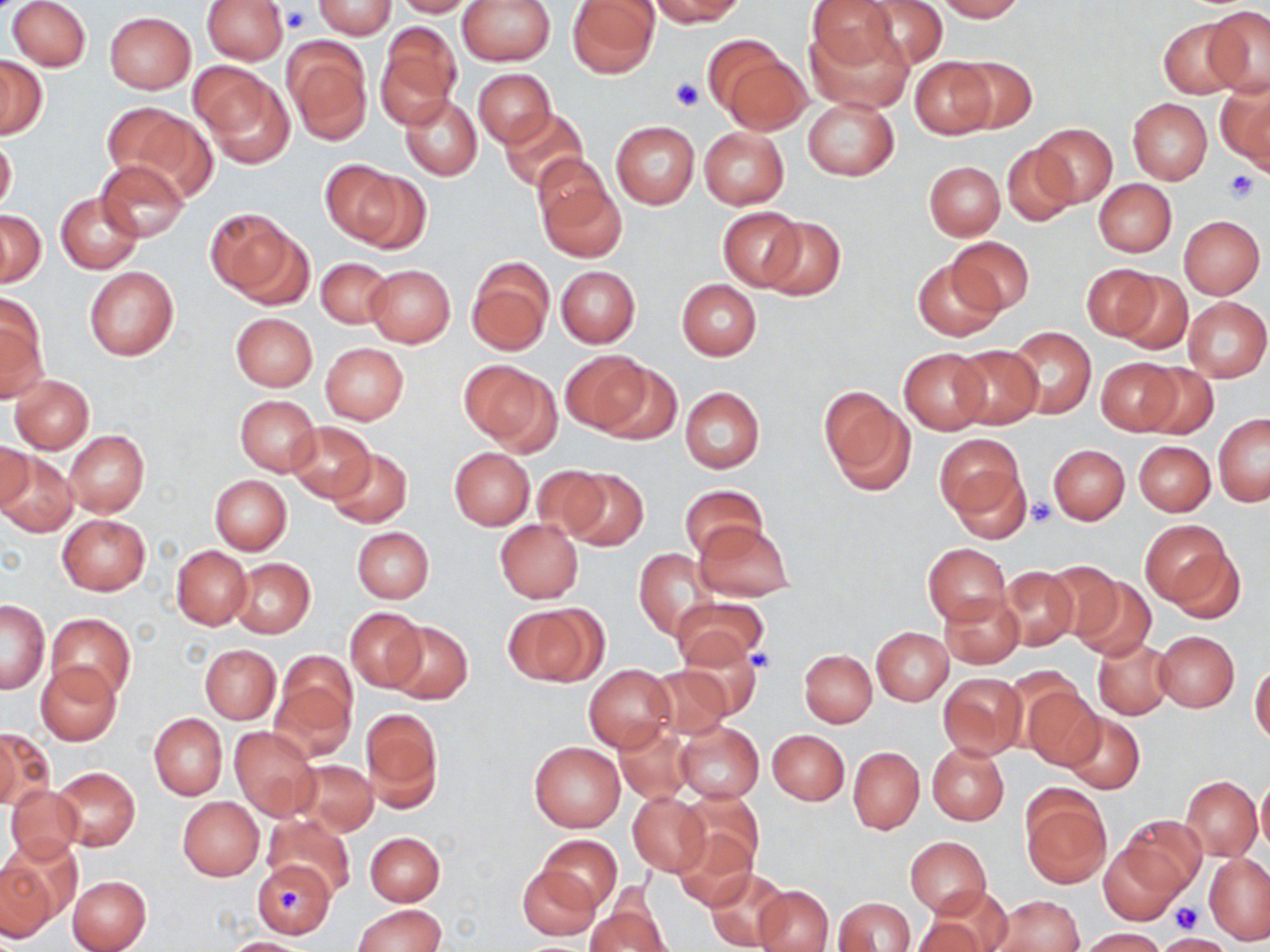

{
  "slide_level_diagnosis": "negative for blood parasites",
  "stain": "May-Grünwald-Giemsa",
  "platelet_locations": "approximate bounding boxes as [x1, y1, x2, y2] in pixels: [282, 8, 311, 34], [671, 77, 702, 112], [1222, 169, 1261, 204], [1028, 498, 1056, 526], [750, 649, 778, 673], [279, 889, 306, 917], [1172, 901, 1204, 932]",
  "uninfected_red_blood_cell_locations": "approximate bounding boxes as [x1, y1, x2, y2] in pixels: [8, 0, 91, 71], [201, 0, 288, 65], [391, 0, 480, 17], [457, 0, 556, 65], [567, 0, 660, 77], [646, 0, 744, 26], [807, 0, 899, 71], [857, 0, 947, 70], [933, 0, 1025, 21], [312, 1, 396, 38], [1201, 6, 1270, 97], [103, 11, 196, 94], [1156, 18, 1248, 99], [376, 21, 461, 124], [805, 21, 914, 114], [284, 40, 373, 146], [703, 40, 802, 131], [951, 54, 1037, 134], [1, 56, 47, 138], [911, 58, 995, 137], [191, 63, 290, 164], [473, 68, 554, 147], [1216, 79, 1270, 171], [401, 95, 481, 180], [803, 97, 899, 181], [1128, 98, 1212, 184], [101, 102, 207, 197], [500, 109, 587, 195], [611, 122, 699, 208], [1030, 123, 1117, 206], [699, 128, 789, 209], [0, 135, 16, 216], [1001, 145, 1080, 227], [533, 155, 612, 232], [97, 160, 188, 242], [924, 161, 1005, 239], [336, 166, 429, 254], [536, 174, 627, 264], [1094, 180, 1177, 256], [55, 192, 142, 274], [719, 208, 805, 290], [0, 210, 45, 286], [211, 213, 310, 307], [1179, 214, 1264, 299], [759, 216, 846, 301], [948, 236, 1034, 315], [316, 257, 392, 328], [912, 258, 1001, 341], [467, 260, 553, 355], [1082, 264, 1158, 341], [364, 265, 455, 348], [556, 266, 639, 347], [85, 267, 178, 360], [1112, 270, 1192, 355], [677, 279, 761, 359], [0, 295, 47, 403], [1182, 296, 1269, 382], [230, 312, 317, 390], [1007, 326, 1096, 419], [320, 343, 408, 423], [951, 344, 1043, 429], [898, 348, 990, 433], [562, 351, 650, 432], [1096, 358, 1181, 435], [458, 361, 559, 451], [1137, 362, 1218, 440], [593, 363, 681, 445], [10, 375, 94, 452], [680, 387, 765, 474], [820, 387, 914, 496], [234, 395, 321, 476], [1213, 415, 1269, 506], [286, 421, 376, 501], [63, 431, 149, 517], [934, 432, 1027, 520], [0, 441, 32, 512], [1134, 441, 1215, 515], [1048, 444, 1130, 524], [449, 447, 535, 530], [327, 448, 413, 527], [2, 451, 78, 538], [530, 466, 613, 541], [563, 468, 649, 551], [951, 469, 1032, 542], [210, 475, 291, 555], [679, 485, 766, 559], [56, 514, 150, 595], [496, 519, 583, 602], [1141, 520, 1239, 615], [693, 521, 795, 602], [352, 527, 433, 602], [923, 543, 1010, 625], [171, 545, 251, 630], [634, 548, 718, 639], [230, 558, 314, 638], [1044, 562, 1131, 648], [997, 565, 1078, 650], [1069, 574, 1156, 662], [939, 592, 1024, 668], [671, 598, 767, 669], [1, 599, 49, 693], [506, 602, 607, 686], [346, 607, 426, 691], [45, 613, 136, 701], [385, 620, 472, 704], [871, 627, 953, 705], [1154, 630, 1239, 711], [1093, 637, 1173, 720], [676, 643, 764, 721], [200, 644, 280, 724], [799, 650, 876, 727], [35, 662, 121, 744], [271, 662, 356, 759], [1250, 663, 1270, 746], [584, 664, 677, 753], [648, 665, 733, 740], [939, 672, 1026, 759], [1023, 686, 1105, 771], [361, 709, 443, 812], [148, 713, 226, 799], [1063, 713, 1144, 794], [675, 721, 764, 802], [614, 722, 692, 803], [229, 726, 319, 819], [2, 728, 50, 810], [767, 729, 848, 804], [529, 741, 625, 832], [927, 742, 1009, 824], [848, 747, 923, 833], [291, 760, 377, 835], [52, 766, 140, 851], [1255, 774, 1270, 856], [1181, 777, 1262, 859], [5, 785, 84, 863], [681, 789, 765, 875], [1020, 789, 1111, 887], [626, 791, 710, 876], [178, 798, 263, 880], [264, 814, 356, 898], [1121, 815, 1205, 895], [673, 828, 757, 911], [365, 831, 444, 905], [539, 835, 622, 909], [3, 836, 84, 925], [906, 837, 991, 915], [1099, 842, 1188, 923], [1204, 854, 1270, 943], [1, 860, 59, 942], [254, 861, 342, 939], [517, 864, 600, 939], [704, 867, 790, 951], [67, 875, 150, 952], [755, 885, 833, 952], [929, 890, 1011, 948], [994, 895, 1083, 952], [836, 898, 914, 951], [586, 901, 671, 952], [352, 904, 446, 952], [912, 914, 990, 952], [1079, 928, 1166, 951], [1158, 933, 1231, 952], [221, 937, 311, 951]",
  "image_size": "1270×952 pixels",
  "preparation": "thin blood film",
  "modality": "optical microscopy",
  "field_of_view": "one of a larger specimen",
  "magnification": "1000x"
}